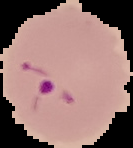
Summary:
  - Image size: 133×148 pixels
  - Malaria status: parasitized
  - Preparation: thin blood smear
  - Image type: cell region segmented out of the field of view; surrounding area masked to black